Locate every Plasmodium parasite and every leukocyte.
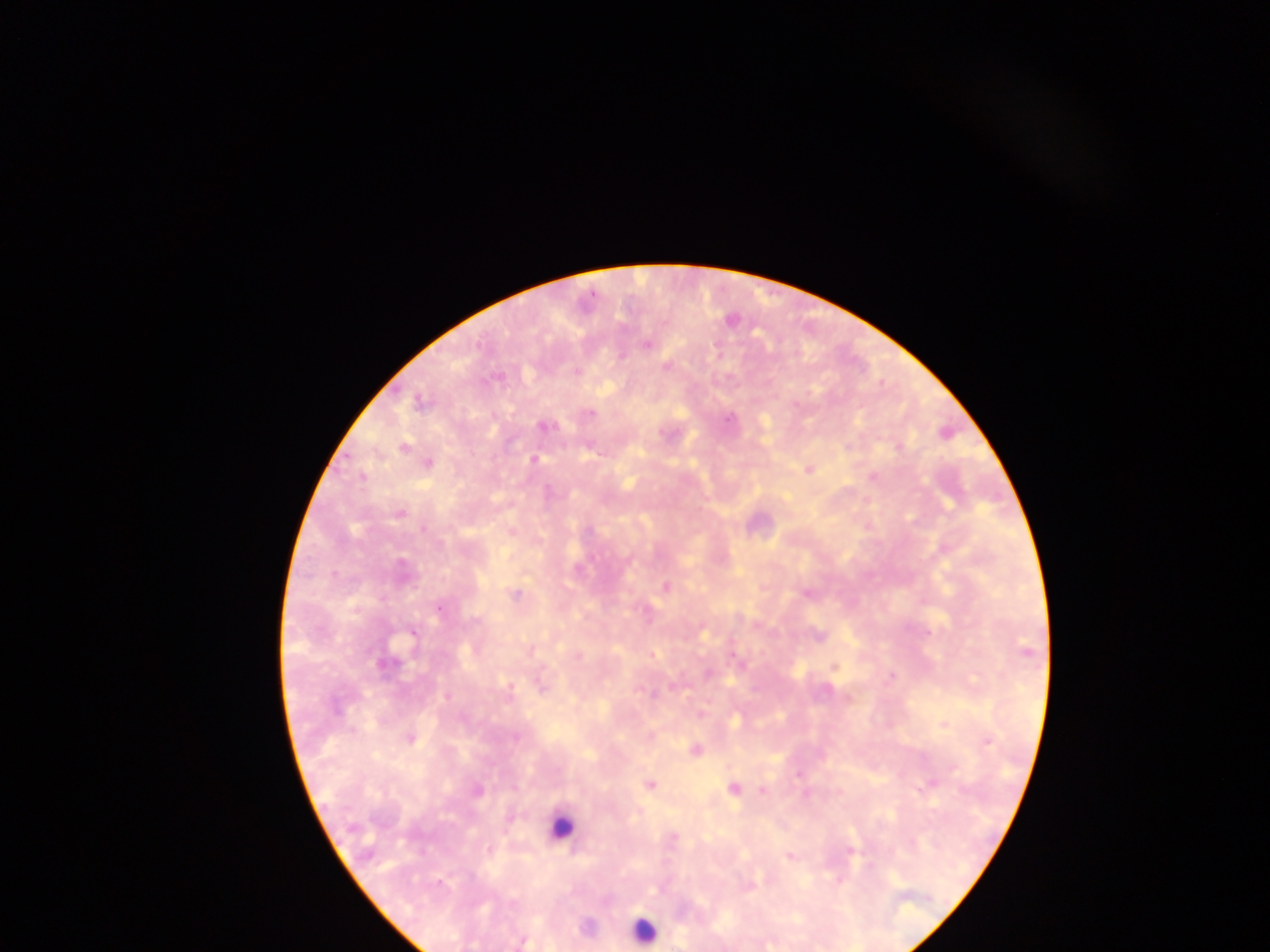
Approximate centers as [x, y] in pixels.
Plasmodium parasites: [731, 320], [647, 344], [667, 366], [576, 372], [419, 403], [591, 413], [729, 419], [543, 426], [404, 447], [899, 447], [593, 450], [534, 459], [428, 464], [808, 469], [362, 476], [873, 477], [399, 514], [423, 530], [589, 531], [401, 564], [665, 587], [806, 593], [515, 595], [439, 609], [475, 620], [412, 636], [1026, 651], [385, 665], [834, 667], [708, 674], [891, 676], [541, 686], [673, 686], [826, 690], [653, 694], [446, 697], [702, 714], [944, 724], [515, 737], [410, 738], [987, 741], [695, 749], [953, 768], [798, 775], [931, 783], [650, 784], [733, 789], [762, 790], [478, 791], [805, 794], [674, 836], [490, 849], [850, 850], [789, 857], [839, 880], [440, 883], [523, 942].
Leukocytes: [560, 827], [643, 930].

image_size: 1270×952 pixels
capture: mobile-phone photograph through a microscope
country: Ghana
field_of_view: single
preparation: thick blood smear